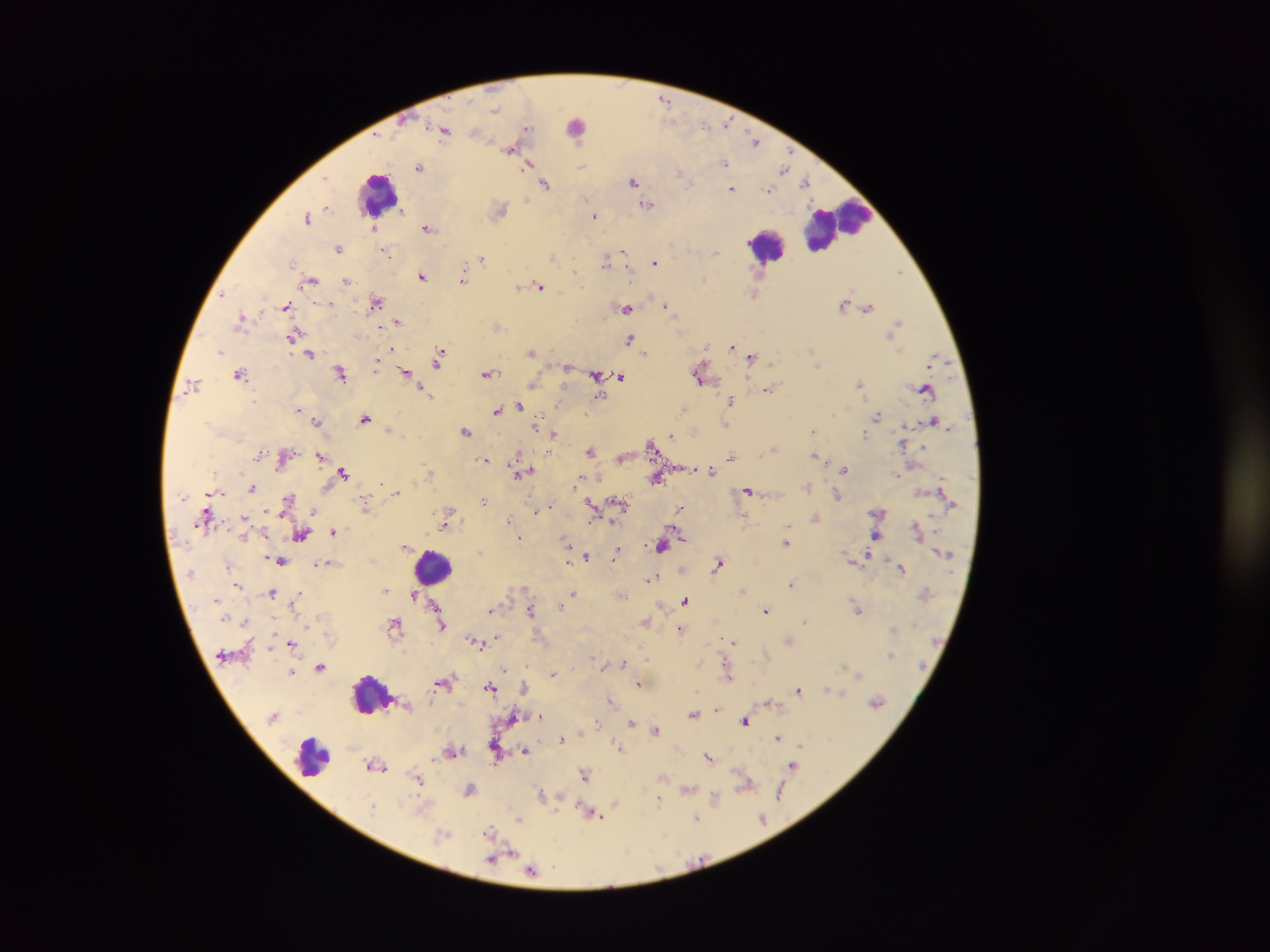
Approximate centers as x y in pixels.
Summary:
  - Plasmodium parasite locations: 665 100; 496 109; 726 122; 526 128; 444 131; 477 133; 754 142; 510 149; 582 162; 725 162; 527 165; 419 167; 783 168; 688 180; 806 181; 633 182; 546 183; 732 189; 768 190; 526 200; 648 204; 327 207; 500 210; 402 211; 594 215; 307 218; 374 228; 427 228; 339 249; 386 251; 623 252; 715 253; 553 256; 482 258; 606 261; 654 262; 899 271; 422 276; 311 280; 462 280; 347 281; 541 286; 519 287; 755 293; 222 295; 377 301; 843 304; 331 305; 667 306; 286 307; 868 307; 627 308; 241 318; 398 321; 898 322; 497 327; 293 335; 629 339; 707 345; 732 346; 391 349; 220 351; 532 351; 645 352; 310 353; 439 357; 752 357; 376 365; 818 366; 566 367; 406 372; 341 373; 240 374; 487 374; 596 375; 621 376; 699 377; 860 383; 534 384; 194 385; 769 389; 926 390; 423 391; 600 396; 731 399; 519 405; 299 409; 684 409; 496 411; 585 414; 878 416; 365 419; 317 421; 726 424; 538 425; 389 429; 466 431; 812 431; 554 434; 864 434; 670 435; 651 446; 773 450; 590 451; 259 454; 815 455; 319 456; 518 456; 731 456; 484 460; 844 469; 524 471; 712 471; 343 472; 518 473; 657 478; 577 483; 807 487; 252 488; 748 490; 396 493; 838 495; 288 499; 484 501; 619 502; 591 505; 366 507; 549 507; 680 509; 536 511; 313 512; 450 512; 879 512; 244 518; 815 518; 508 520; 445 525; 788 527; 334 531; 302 535; 876 536; 520 538; 567 542; 786 543; 406 545; 662 545; 479 553; 616 555; 587 556; 568 560; 281 561; 319 564; 718 564; 228 566; 902 568; 652 578; 791 583; 237 585; 385 590; 742 590; 271 592; 573 593; 412 594; 298 597; 686 600; 295 601; 435 605; 560 606; 858 609; 531 610; 766 610; 491 611; 805 620; 245 622; 646 622; 395 624; 442 626; 681 629; 497 637; 789 640; 475 641; 733 642; 291 643; 890 655; 592 658; 624 662; 321 667; 505 670; 292 672; 553 674; 859 674; 729 675; 639 684; 490 687; 524 687; 827 688; 799 690; 842 694; 610 700; 769 701; 877 702; 718 708; 693 714; 541 717; 745 721; 597 723; 632 723; 655 730; 778 738; 562 740; 617 744; 801 746; 620 748; 453 750; 525 750; 709 757; 433 758; 377 765; 793 766; 585 774; 418 779; 746 784; 469 789; 688 789; 541 794; 780 794; 715 798; 659 801; 615 804; 372 807; 594 815; 696 818; 519 819; 762 819; 490 831; 443 835; 512 852; 491 860; 532 870
  - Leukocyte locations: 582 124; 377 191; 837 225; 766 246; 433 567; 370 694; 312 757
  - Image size: 1270×952 pixels
  - Preparation: thick blood smear
  - Field of view: single
  - Country: Ghana
  - Capture: mobile-phone photograph through a microscope